Classify this cell by malaria status.
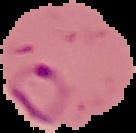

Parasitized.

preparation = thin blood smear
image size = 136×133 pixels
image type = cell region segmented out of the field of view; surrounding area masked to black